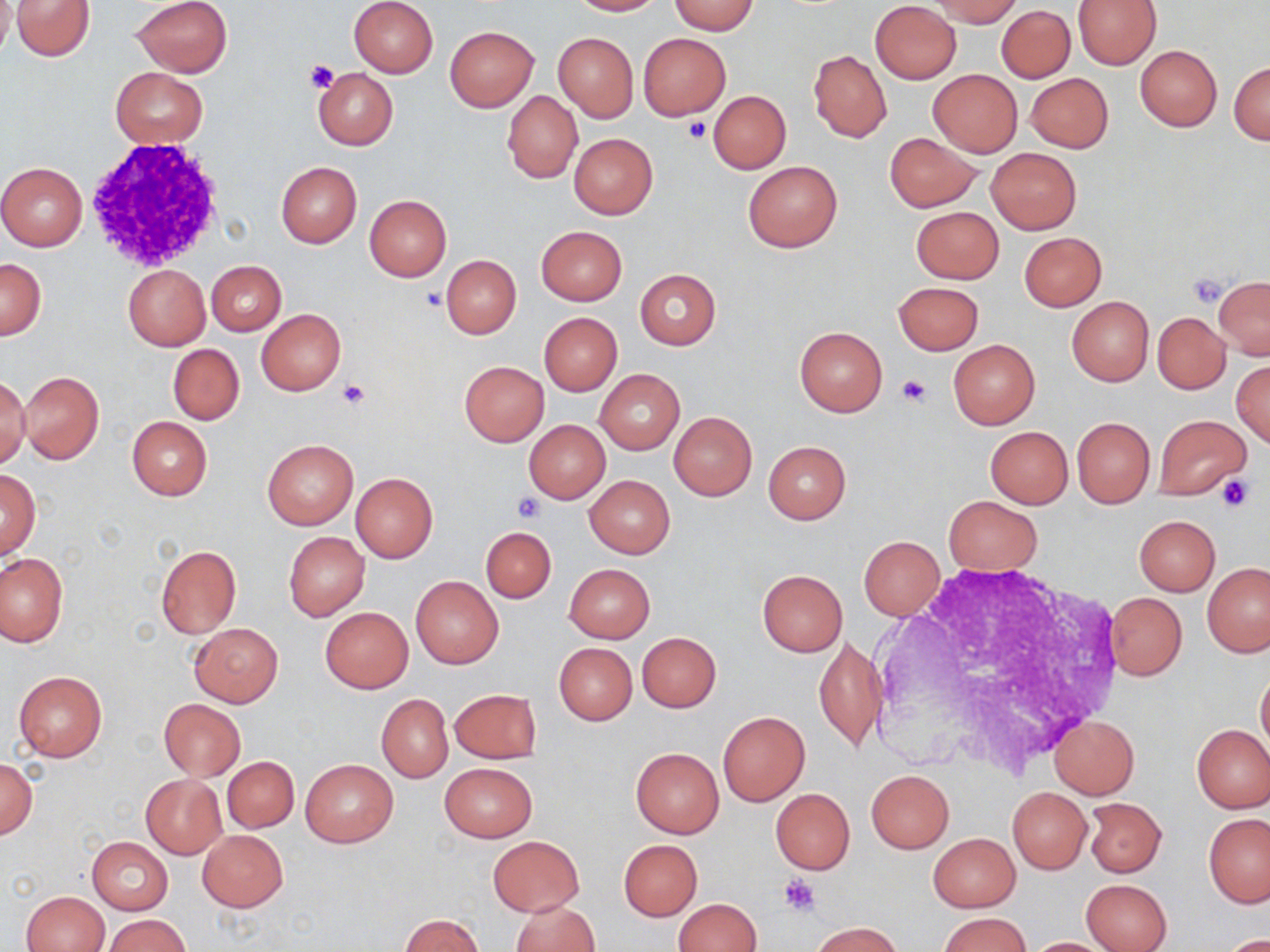

Summary:
  - Coordinate format: approximate bounding boxes as [x1, y1, x2, y2] in pixels
  - White blood cell locations: [84, 139, 236, 274]
  - Uninfected red blood cell locations: [0, 0, 15, 58], [10, 0, 96, 61], [131, 0, 233, 77], [348, 0, 438, 78], [567, 0, 660, 16], [930, 0, 1022, 26], [669, 1, 759, 35], [870, 1, 961, 83], [1071, 1, 1161, 69], [997, 5, 1075, 83], [445, 25, 538, 111], [553, 32, 638, 122], [638, 33, 730, 120], [1135, 46, 1221, 131], [807, 51, 893, 143], [1229, 60, 1269, 145], [313, 67, 398, 150], [111, 68, 207, 148], [927, 69, 1023, 157], [1026, 73, 1113, 152], [502, 90, 583, 183], [709, 91, 790, 174], [569, 133, 658, 219], [885, 133, 980, 212], [986, 148, 1081, 233], [276, 161, 361, 247], [743, 161, 842, 252], [0, 163, 88, 252], [364, 195, 451, 281], [910, 206, 1003, 283], [536, 225, 627, 305], [1019, 232, 1107, 311], [441, 254, 522, 339], [0, 257, 47, 340], [207, 260, 286, 336], [122, 265, 210, 350], [635, 269, 720, 350], [1213, 277, 1270, 358], [894, 281, 983, 354], [1067, 297, 1154, 386], [257, 308, 346, 395], [539, 312, 622, 395], [1152, 312, 1229, 393], [794, 326, 888, 416], [949, 340, 1040, 429], [168, 344, 244, 424], [1232, 360, 1270, 446], [459, 361, 548, 445], [18, 370, 104, 465], [596, 370, 683, 453], [0, 374, 31, 471], [669, 411, 757, 500], [1154, 414, 1250, 500], [127, 416, 212, 501], [1072, 417, 1154, 508], [524, 420, 610, 503], [984, 426, 1073, 508], [262, 437, 359, 530], [763, 440, 851, 523], [0, 469, 41, 560], [350, 473, 437, 563], [585, 475, 675, 558], [943, 496, 1042, 575], [1134, 515, 1220, 596], [481, 527, 556, 603], [283, 531, 369, 621], [858, 535, 944, 619], [155, 545, 241, 637], [0, 553, 67, 648], [563, 563, 655, 643], [1203, 563, 1270, 656], [757, 569, 848, 656], [411, 576, 503, 668], [1104, 592, 1187, 681], [321, 606, 413, 692], [189, 623, 283, 707], [636, 631, 721, 712], [814, 636, 888, 752], [554, 643, 636, 725], [1256, 668, 1269, 755], [13, 671, 107, 761], [448, 689, 540, 764], [377, 693, 453, 782], [159, 698, 246, 779], [718, 712, 809, 805], [1048, 716, 1139, 799], [1192, 724, 1270, 812], [631, 748, 724, 837], [222, 756, 298, 832], [0, 757, 37, 840], [300, 759, 397, 849], [440, 762, 537, 843], [866, 770, 953, 853], [141, 774, 226, 858], [1008, 786, 1092, 874], [771, 788, 855, 874], [1083, 797, 1166, 878], [1203, 814, 1270, 907], [198, 829, 287, 911], [929, 834, 1020, 911], [87, 836, 172, 915], [487, 836, 584, 915], [619, 839, 702, 920], [1081, 878, 1172, 952], [21, 891, 108, 952], [673, 898, 761, 952], [512, 901, 599, 952], [939, 913, 1029, 952], [105, 914, 191, 952], [401, 915, 484, 952], [811, 921, 903, 952], [1217, 933, 1270, 952], [1023, 937, 1117, 951]
  - Platelet locations: [304, 59, 337, 93], [684, 117, 712, 143], [1188, 272, 1231, 307], [420, 285, 446, 311], [897, 375, 931, 407], [338, 378, 368, 409], [1216, 473, 1256, 514], [514, 493, 543, 522], [779, 874, 822, 916]
  - Slide-level diagnosis: no evidence of blood parasites
  - Preparation: thin blood smear
  - Magnification: 1000x
  - Image size: 1270×952 pixels
  - Stain: May-Grünwald-Giemsa
  - Modality: optical microscopy
  - Field of view: single